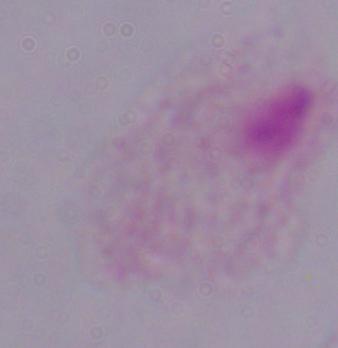 A trichomonad is seen. 1000x magnification. Micrograph.